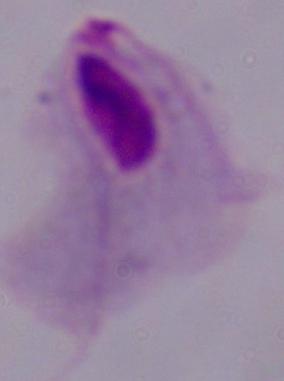
{
  "identification": "trichomonad",
  "modality": "photomicrograph",
  "magnification": "1000x"
}